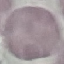
{
  "malaria_status": "uninfected",
  "stain": "Giemsa",
  "image_type": "automatically extracted cell patch, resized to 64 × 64 pixels",
  "capture": "smartphone through the microscope eyepiece",
  "preparation": "thin blood film"
}